Assess for malaria.
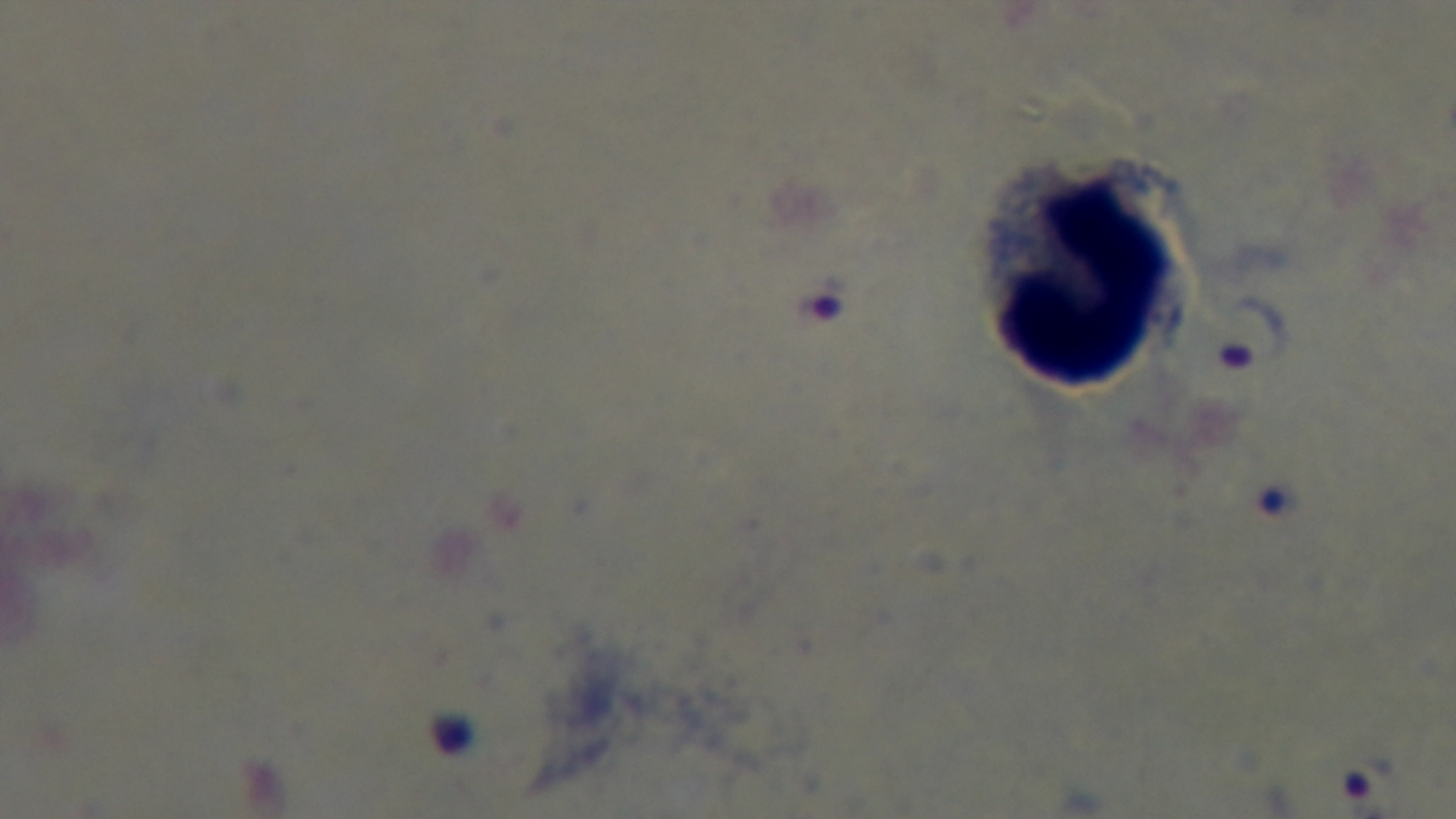

Infected.

Captured with a mounted 4K digital camera. Giemsa stain. Oil-immersion objective, 100x. One field from the slide. Photomicrograph. Preparation: thick.